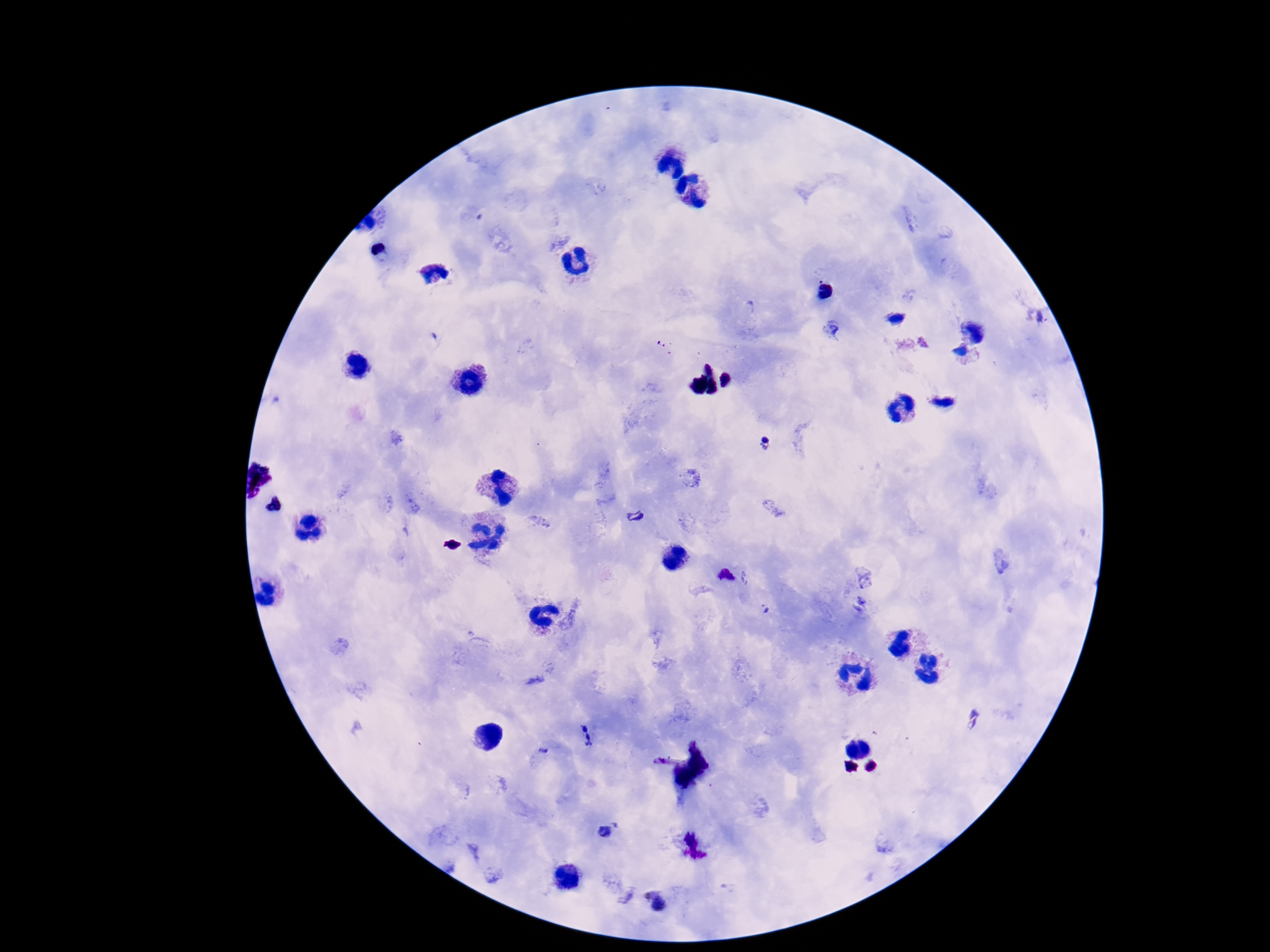
plasmodium_parasite_locations: 'approximate centers as (x, y) in pixels: (767, 443), (635, 517), (725, 577), (587, 734), (606, 832), (655, 900)'
capture: smartphone camera through the microscope eyepiece
field_of_view: one from this slide
magnification: 100x
image_size: 1270×952 pixels
patient_malaria_status: infected
preparation: thick peripheral-blood smear
stain: Giemsa